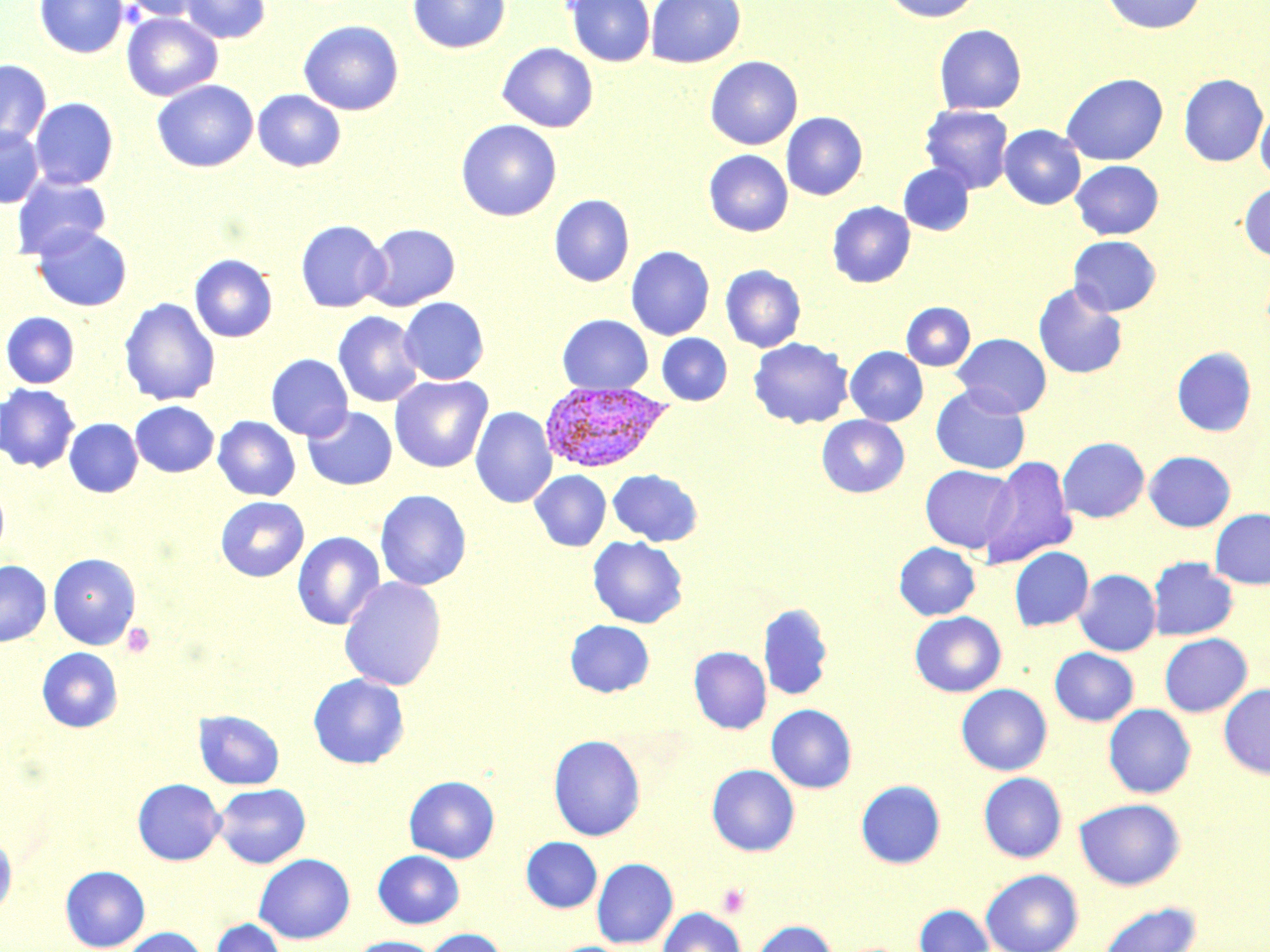
Summary:
  - Coordinate format: approximate bounding boxes as (x1, y1, x2, y2) in pixels
  - Plasmodium vivax-infected red blood cell locations: (539, 382, 672, 473)
  - Uninfected red blood cell locations: (35, 0, 128, 58), (118, 0, 208, 21), (180, 0, 270, 43), (407, 0, 511, 54), (564, 0, 655, 67), (645, 0, 745, 68), (881, 0, 983, 22), (1100, 0, 1207, 34), (121, 13, 222, 101), (298, 19, 404, 115), (934, 24, 1026, 114), (497, 42, 598, 132), (705, 56, 803, 149), (0, 59, 51, 149), (1060, 73, 1168, 166), (1179, 74, 1268, 167), (152, 80, 258, 172), (253, 89, 346, 172), (29, 97, 119, 189), (920, 105, 1014, 194), (1255, 105, 1270, 182), (781, 111, 868, 200), (456, 119, 562, 221), (999, 125, 1086, 209), (0, 126, 44, 208), (703, 150, 793, 236), (1071, 160, 1163, 239), (898, 164, 974, 236), (11, 174, 112, 260), (1239, 182, 1270, 261), (549, 194, 635, 286), (827, 201, 915, 288), (295, 220, 389, 312), (363, 223, 461, 311), (32, 225, 132, 311), (1068, 235, 1160, 315), (626, 246, 715, 340), (189, 253, 278, 342), (721, 264, 806, 352), (1033, 282, 1128, 379), (119, 297, 220, 405), (399, 297, 489, 385), (901, 302, 975, 370), (1, 311, 80, 388), (333, 311, 424, 408), (558, 315, 652, 394), (657, 333, 732, 405), (952, 333, 1052, 417), (748, 337, 853, 429), (845, 346, 928, 426), (1172, 347, 1256, 437), (266, 354, 353, 441), (390, 375, 493, 473), (0, 383, 80, 473), (930, 384, 1031, 474), (130, 401, 219, 477), (471, 406, 557, 508), (303, 407, 397, 490), (816, 415, 909, 498), (213, 416, 300, 501), (64, 418, 143, 497), (1058, 437, 1149, 523), (1144, 450, 1236, 532), (979, 455, 1077, 569), (920, 465, 1018, 552), (608, 469, 703, 546), (530, 470, 611, 551), (0, 480, 10, 560), (375, 489, 471, 591), (216, 496, 309, 582), (1210, 508, 1270, 589), (292, 531, 385, 630), (588, 536, 688, 628), (894, 542, 980, 620), (1009, 547, 1094, 630), (48, 552, 141, 649), (1147, 557, 1238, 640), (0, 560, 51, 646), (1074, 569, 1161, 656), (339, 576, 446, 691), (758, 603, 834, 701), (909, 611, 1006, 697), (565, 619, 655, 697), (1159, 633, 1252, 716), (689, 646, 771, 734), (37, 647, 123, 732), (1049, 648, 1138, 726), (308, 673, 410, 769), (1218, 683, 1270, 778), (956, 684, 1052, 775), (766, 704, 857, 793), (1103, 704, 1196, 798), (194, 710, 285, 789), (548, 734, 646, 841), (706, 764, 799, 855), (978, 772, 1067, 862), (404, 775, 500, 863), (132, 778, 226, 865), (855, 780, 945, 869), (213, 783, 311, 868), (1074, 798, 1184, 890), (0, 834, 17, 919), (521, 837, 602, 913), (373, 850, 464, 928), (254, 853, 355, 944), (591, 858, 679, 948), (60, 865, 150, 951), (980, 868, 1084, 952), (1097, 902, 1202, 952), (914, 904, 994, 952), (658, 907, 746, 952), (211, 918, 286, 952), (751, 919, 837, 952), (119, 926, 209, 952), (420, 928, 508, 952), (349, 936, 439, 952)
  - Platelet locations: (122, 623, 155, 658), (716, 883, 750, 918)
  - Slide-level diagnosis: Plasmodium vivax
  - Stain: May-Grünwald-Giemsa
  - Image size: 1270×952 pixels
  - Magnification: 1000x
  - Preparation: thin blood smear
  - Modality: light microscopy
  - Field of view: single